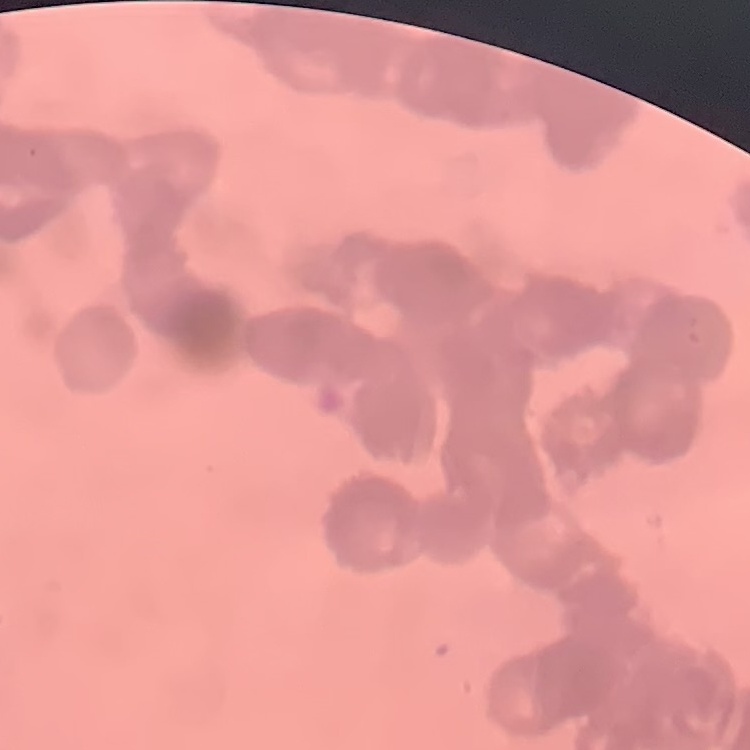

red blood cell morphology = rouleaux formation
preparation = thin blood smear
stain = Field's or Giemsa
image type = one tile cut from a larger photomicrograph